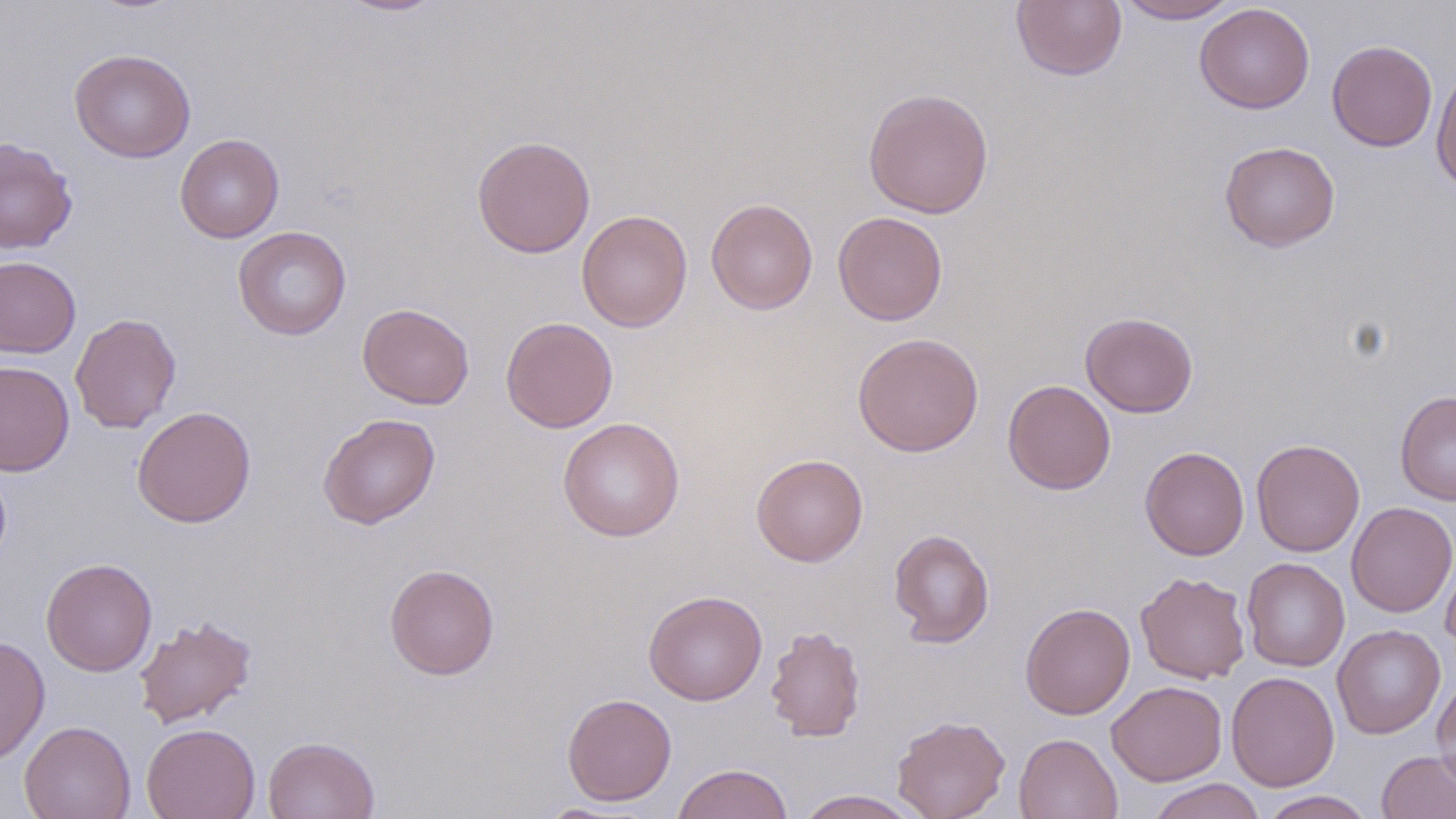

slide-level diagnosis = no evidence of blood parasites
preparation = thin blood smear
magnification = 1000x
stain = May-Grünwald-Giemsa
uninfected red blood cell locations = approximate bounding boxes as (x1,y1)-(x2,y2) corner pairs in pixels: (334,0)-(448,16), (1011,0)-(1128,82), (1115,0)-(1241,23), (1194,3)-(1314,114), (1327,39)-(1437,152), (69,48)-(196,163), (1431,66)-(1456,195), (863,87)-(994,219), (175,134)-(285,243), (472,135)-(596,258), (0,137)-(78,254), (1219,140)-(1340,252), (706,198)-(818,314), (576,210)-(693,332), (833,211)-(948,325), (233,226)-(351,340), (0,255)-(82,358), (357,303)-(474,409), (1080,311)-(1198,418), (70,313)-(182,433), (501,316)-(618,433), (852,332)-(984,457), (0,360)-(75,476), (1003,379)-(1116,494), (1395,390)-(1456,506), (131,406)-(256,528), (317,413)-(440,529), (557,418)-(685,542), (1251,439)-(1365,557), (1139,446)-(1250,560), (751,453)-(868,567), (1345,501)-(1456,618), (888,528)-(995,648), (1440,542)-(1456,654), (1241,557)-(1350,672), (41,558)-(157,676), (384,563)-(500,680), (1136,571)-(1251,684), (643,590)-(768,705), (1020,602)-(1135,720), (134,615)-(257,729), (764,624)-(867,743), (1332,624)-(1446,739), (0,635)-(50,764), (1226,670)-(1339,791), (1432,674)-(1456,793), (1107,681)-(1227,786), (561,692)-(677,806), (892,714)-(1011,819), (19,720)-(136,819), (142,723)-(260,819), (1013,733)-(1123,819), (263,735)-(379,819), (1376,749)-(1456,819), (671,763)-(794,819), (1146,778)-(1266,819), (795,789)-(922,818), (1258,790)-(1375,819)
field of view = one of a larger specimen
image size = 1456×819 pixels
modality = optical microscopy